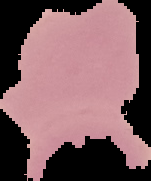
Summary:
  - Image type: cell region segmented out of the field of view; surrounding area masked to black
  - Image size: 151×181 pixels
  - Preparation: thin blood film
  - Malaria status: uninfected